Report the malaria status of this cell.
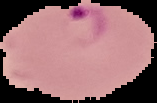
It is parasitized.

image size = 157×103 pixels
image type = cell region segmented out of the field of view; surrounding area masked to black
preparation = thin blood smear